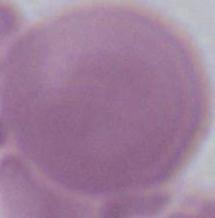

magnification: 1000x
identification: red blood cell
modality: photomicrograph